Give the preparation type.
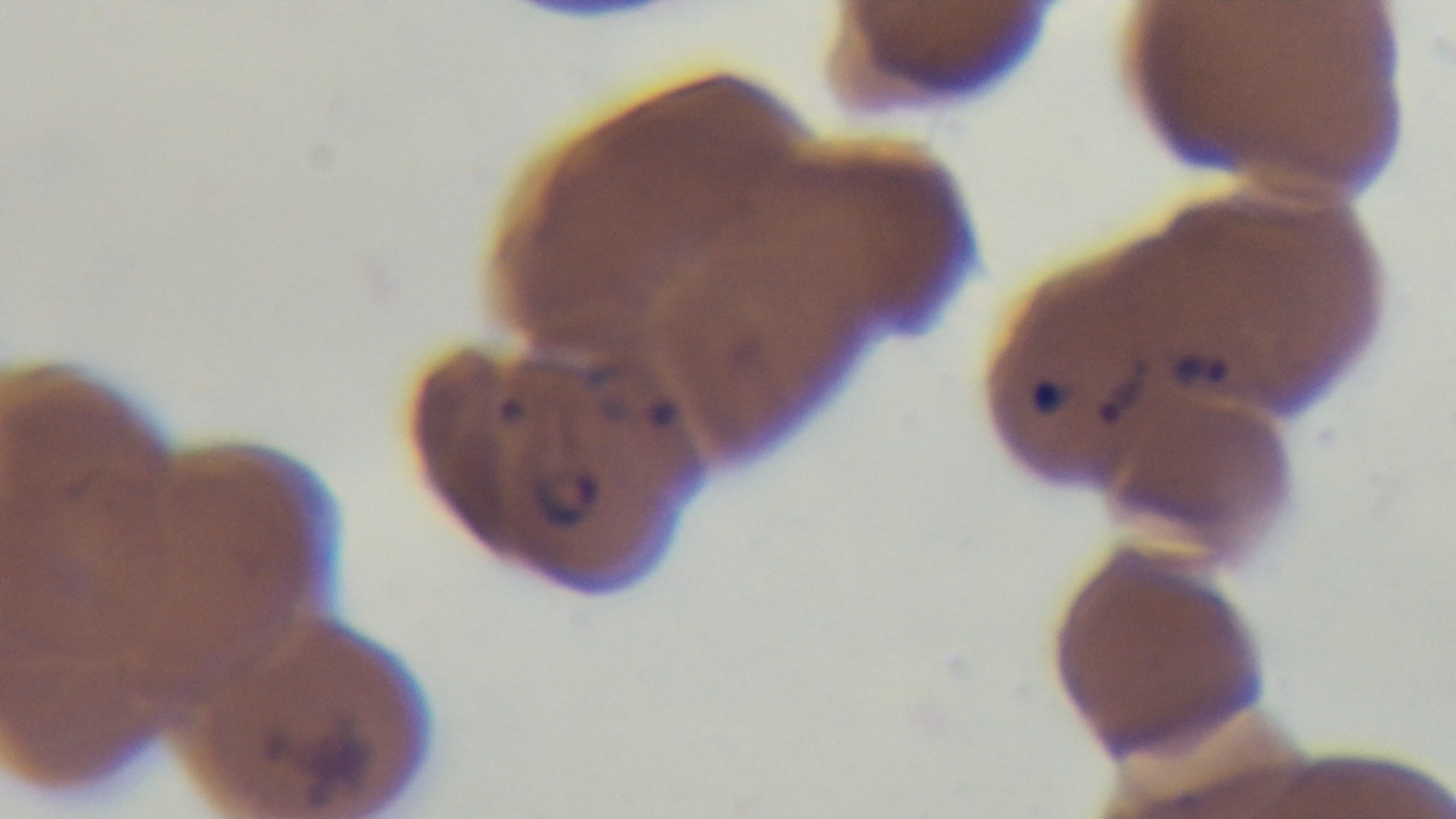
It is a thin blood film.

objective = 100x oil immersion
capture = mounted 4K digital camera
modality = light microscopy
stain = Giemsa
malaria status = positive
field of view = one from the slide